Identify the preparation type.
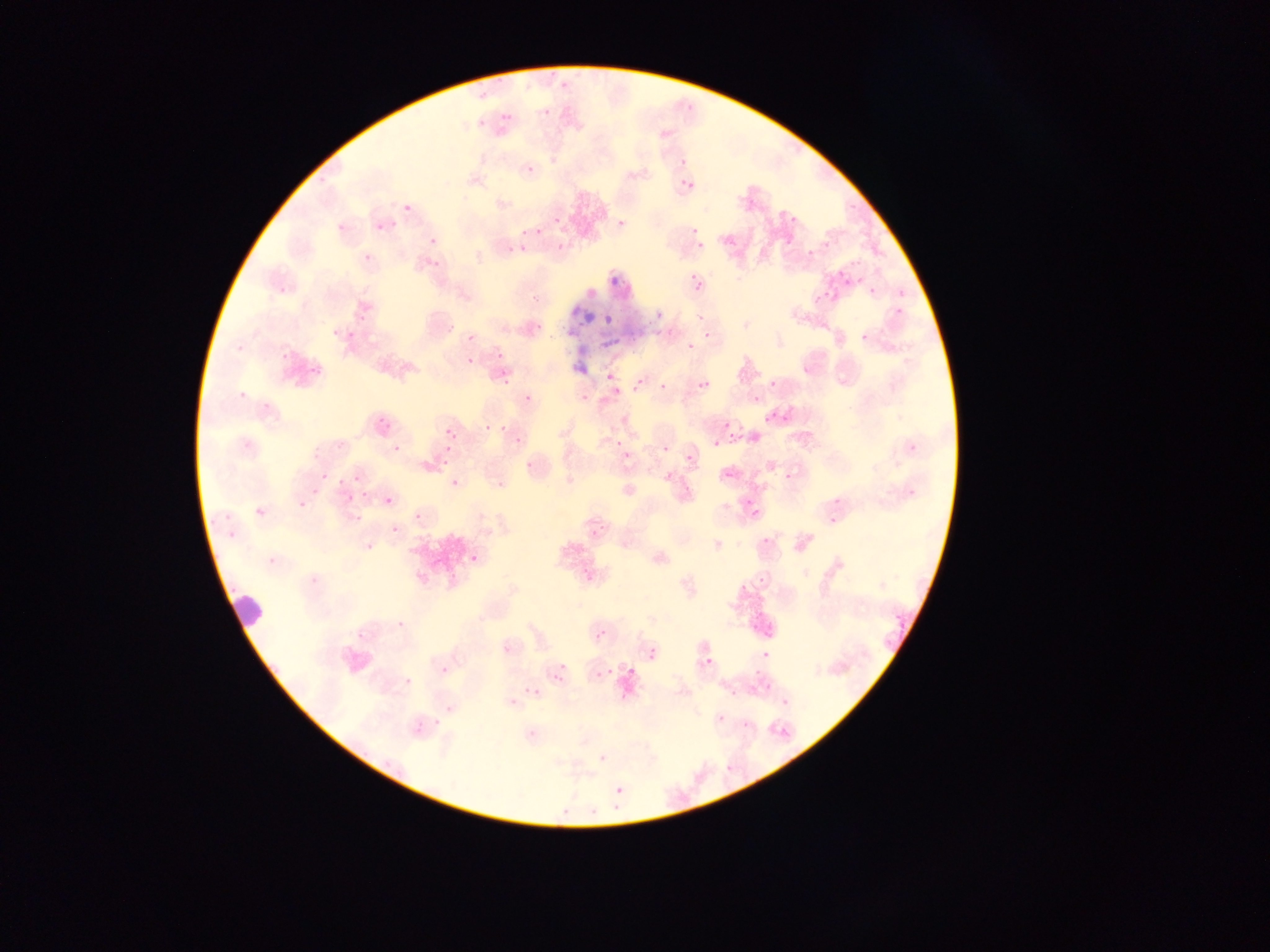

Thin blood film.

Approximate bounding boxes as {left, top, right, bottom} in pixels. Plasmodium parasite locations (subset; some below the resolvable size): {556, 79, 572, 89}, {478, 89, 486, 98}, {500, 111, 513, 123}, {478, 115, 486, 128}, {678, 158, 686, 163}, {526, 165, 540, 173}, {679, 182, 692, 192}, {552, 217, 562, 222}, {618, 220, 626, 225}, {536, 224, 543, 234}, {519, 229, 527, 237}, {689, 230, 697, 235}, {697, 241, 708, 248}, {507, 243, 518, 253}, {519, 245, 530, 251}, {849, 257, 864, 267}, {610, 270, 617, 286}, {856, 273, 865, 282}, {688, 274, 703, 284}, {840, 275, 852, 283}, {692, 282, 703, 291}, {869, 286, 875, 294}, {814, 292, 827, 308}, {654, 308, 664, 318}, {604, 314, 618, 322}, {348, 329, 354, 339}, {603, 334, 623, 347}, {605, 370, 618, 381}, {697, 378, 711, 387}, {630, 379, 643, 391}, {656, 380, 668, 390}, {769, 381, 780, 386}, {753, 393, 759, 401}, {763, 410, 776, 421}, {783, 415, 792, 423}, {379, 419, 387, 424}, {384, 423, 396, 431}, {501, 425, 508, 433}, {726, 432, 739, 444}, {451, 433, 460, 441}, {712, 440, 720, 449}, {443, 447, 454, 452}, {353, 475, 363, 482}, {337, 478, 348, 484}, {451, 479, 459, 488}, {347, 494, 357, 502}, {384, 497, 394, 504}, {416, 511, 428, 521}, {471, 552, 479, 560}, {591, 626, 606, 639}, {644, 643, 660, 660}, {552, 658, 571, 684}, {604, 660, 618, 676}, {595, 672, 603, 679}, {522, 681, 543, 696}, {432, 718, 445, 727}, {413, 721, 426, 730}, {611, 789, 624, 797} | approximate {x, y} pixel centers of objects too small to bound: {407, 207}, {434, 241}, {468, 361}, {487, 427}, {447, 431}, {619, 443}, {446, 463}. Leukocyte locations: {578, 306, 599, 328}, {568, 341, 597, 373}, {218, 590, 266, 629}. Image is 1270×952 pixels. Mobile-phone photograph taken through the microscope. Collected in Ghana. Single field of view.